State the blood parasite species.
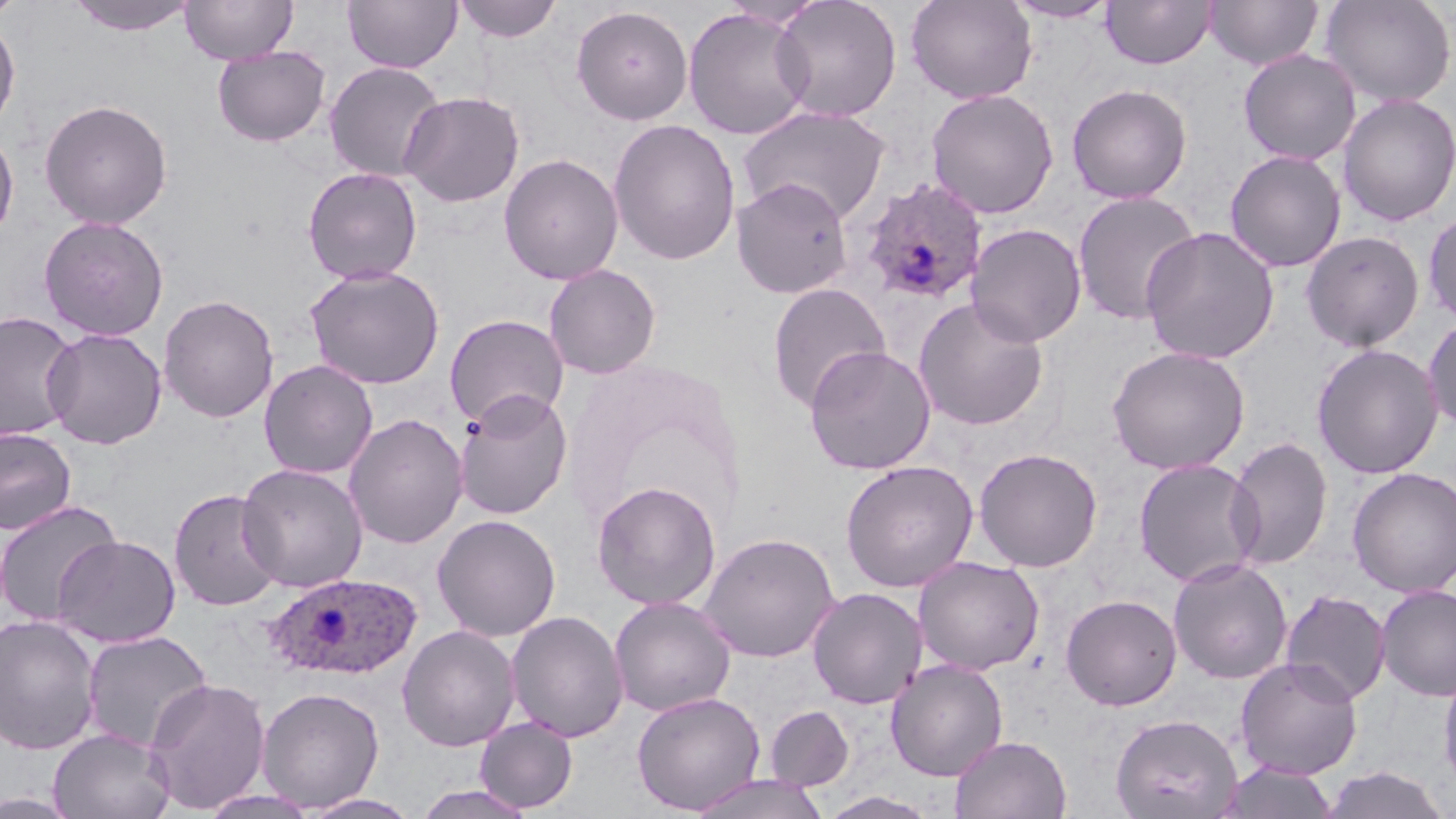

Plasmodium ovale.

Approximate bounding boxes as (x1,y1)-(x2,y2) corner pairs in pixels. Plasmodium ovale-infected red blood cell locations: (858,177)-(989,305), (267,572)-(424,681). Uninfected red blood cell locations: (0,0)-(27,23), (66,0)-(199,36), (180,0)-(298,65), (342,0)-(462,74), (453,0)-(564,43), (770,0)-(902,122), (905,0)-(1038,104), (1002,0)-(1120,23), (1100,0)-(1215,70), (1204,0)-(1322,70), (1321,0)-(1455,107), (571,4)-(694,125), (683,8)-(814,140), (0,15)-(21,135), (212,46)-(331,147), (1238,49)-(1360,165), (324,61)-(447,182), (1066,83)-(1192,204), (926,88)-(1059,219), (399,91)-(525,207), (1337,92)-(1456,226), (39,98)-(173,229), (737,105)-(892,224), (608,118)-(741,266), (0,128)-(19,242), (1224,150)-(1346,273), (498,153)-(624,285), (302,167)-(423,285), (731,177)-(854,299), (1071,190)-(1200,326), (1422,208)-(1456,327), (39,216)-(169,341), (966,223)-(1087,347), (1141,226)-(1280,365), (1301,230)-(1424,352), (543,263)-(661,380), (304,265)-(446,389), (767,282)-(891,410), (158,294)-(279,423), (913,297)-(1050,431), (0,312)-(80,442), (444,314)-(569,428), (1423,315)-(1456,433), (41,328)-(167,449), (1311,344)-(1444,480), (804,345)-(936,474), (1107,346)-(1250,474), (258,359)-(378,479), (454,388)-(574,520), (344,413)-(468,549), (0,426)-(77,535), (1225,437)-(1333,569), (973,447)-(1103,572), (1132,458)-(1263,587), (839,459)-(979,592), (236,463)-(368,592), (1347,467)-(1456,598), (591,480)-(722,610), (168,487)-(284,611), (0,499)-(122,628), (431,514)-(561,641), (699,532)-(839,662), (52,534)-(181,648), (914,556)-(1044,674), (1168,557)-(1293,684), (1375,584)-(1456,700), (807,587)-(927,709), (1280,589)-(1391,705), (1061,593)-(1182,710), (609,596)-(736,717), (506,610)-(629,742), (0,615)-(102,755), (396,624)-(521,751), (81,630)-(213,752), (1235,656)-(1363,780), (885,659)-(1008,781), (1438,662)-(1456,796), (143,677)-(271,814), (256,686)-(385,812), (631,691)-(765,814), (765,705)-(854,791), (1110,713)-(1242,819), (474,716)-(578,813), (49,727)-(175,819), (950,735)-(1072,818), (1216,760)-(1341,819), (1319,767)-(1451,818), (687,774)-(832,819), (411,784)-(537,819), (198,789)-(320,819), (819,791)-(940,819), (299,793)-(424,819). Thin blood film. Image is 1456×819 pixels. May-Grünwald-Giemsa-stained preparation. 1000x magnification. One field of a larger specimen. Optical microscopy.